Comment on the morphology of the red blood cells.
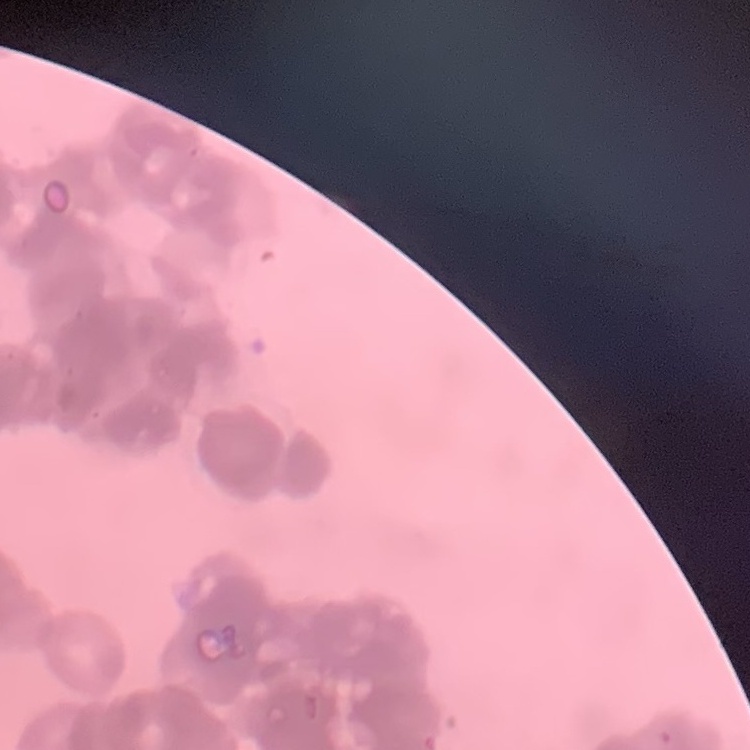
They show rouleaux formation.

Summary:
  - Image type: one tile cut from a larger photomicrograph
  - Stain: Field's or Giemsa
  - Preparation: thin blood film